Describe the morphology of the red blood cells.
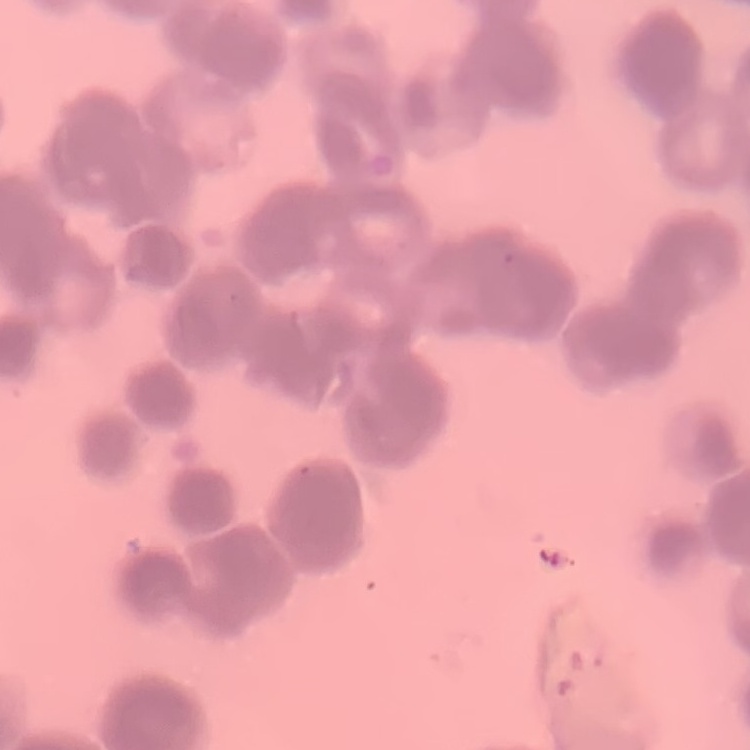
They show rouleaux formation.

{
  "preparation": "thin blood smear",
  "image_type": "one tile cut from a larger photomicrograph",
  "stain": "Field's or Giemsa"
}